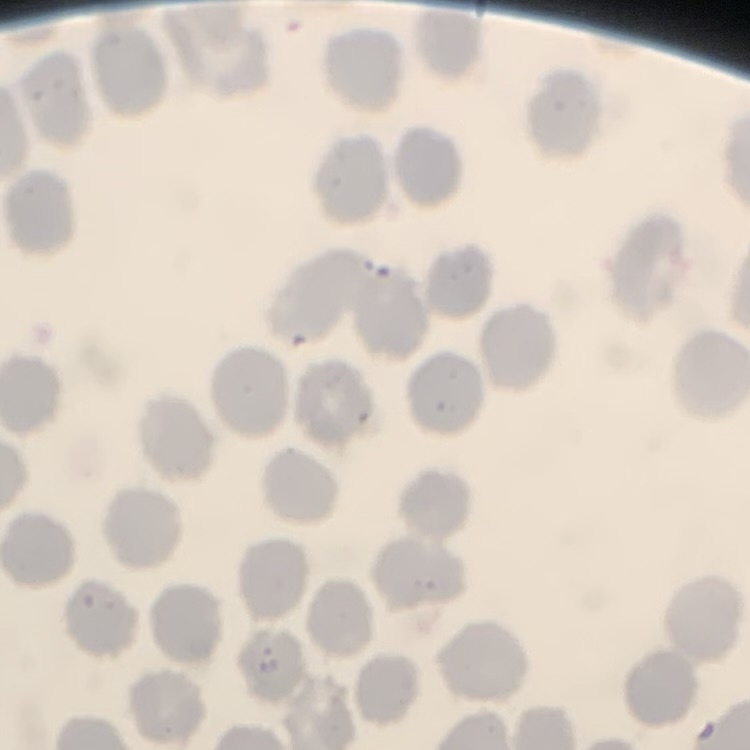
erythrocyte morphology = no rouleaux formation
stain = Field's or Giemsa
image type = one tile cut from a larger photomicrograph
preparation = thin peripheral smear